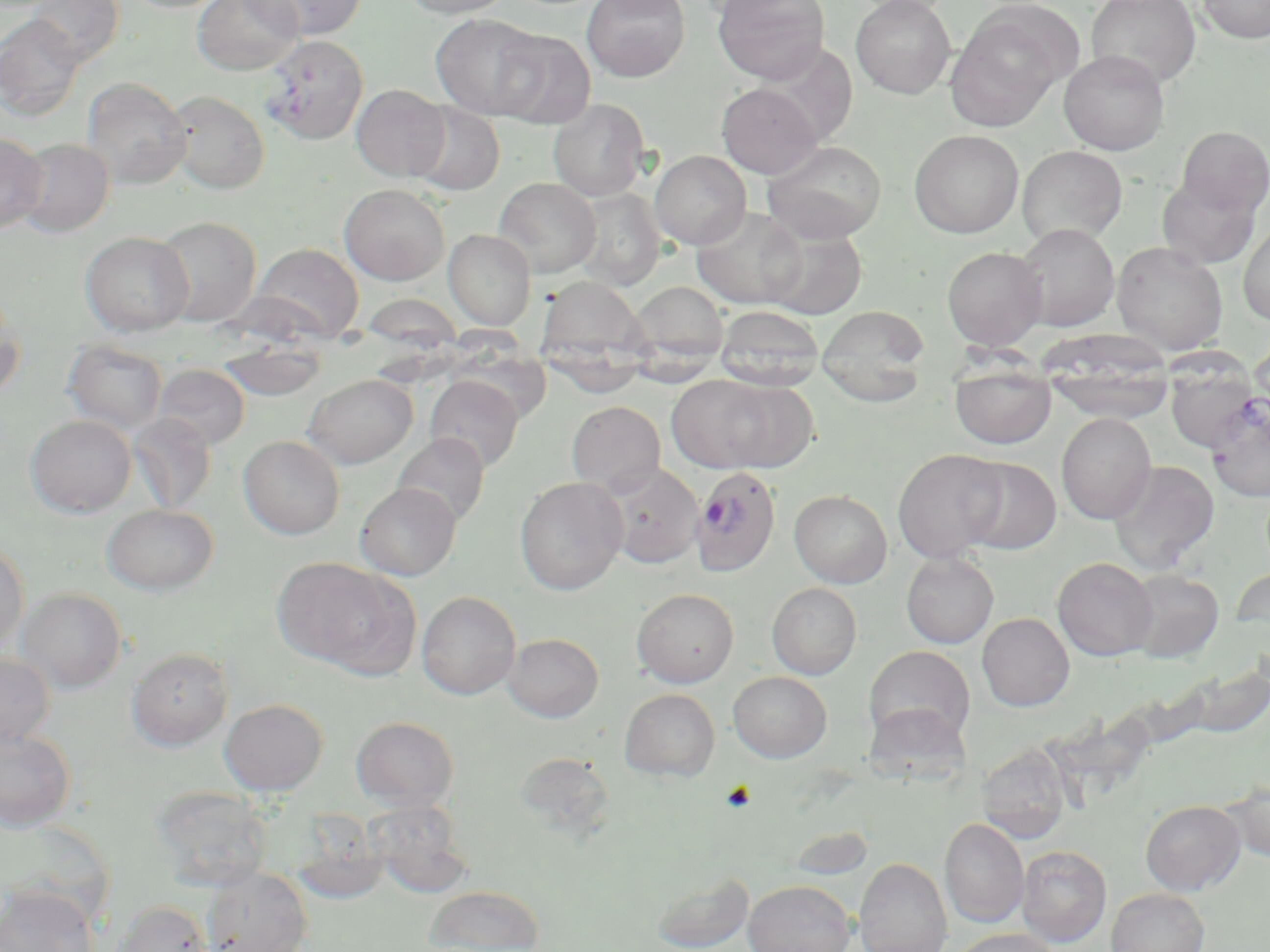

Approximate bounding boxes as named x1/y1/x2/y2 corners in pixels. Platelet locations: (x1=720, y1=781, x2=756, y2=812). Plasmodium falciparum-infected red blood cell locations: (x1=691, y1=466, x2=781, y2=576). Uninfected red blood cell locations: (x1=24, y1=0, x2=124, y2=67), (x1=193, y1=0, x2=303, y2=75), (x1=246, y1=0, x2=366, y2=40), (x1=400, y1=0, x2=514, y2=19), (x1=581, y1=0, x2=690, y2=82), (x1=594, y1=0, x2=689, y2=18), (x1=713, y1=0, x2=830, y2=84), (x1=850, y1=0, x2=956, y2=99), (x1=1087, y1=0, x2=1201, y2=89), (x1=1197, y1=0, x2=1270, y2=43), (x1=945, y1=7, x2=1072, y2=129), (x1=1, y1=13, x2=85, y2=121), (x1=430, y1=13, x2=547, y2=120), (x1=490, y1=29, x2=596, y2=129), (x1=260, y1=36, x2=368, y2=144), (x1=752, y1=48, x2=858, y2=152), (x1=1058, y1=50, x2=1170, y2=155), (x1=82, y1=78, x2=192, y2=189), (x1=717, y1=83, x2=822, y2=179), (x1=351, y1=84, x2=451, y2=181), (x1=165, y1=90, x2=270, y2=194), (x1=548, y1=99, x2=650, y2=201), (x1=409, y1=102, x2=505, y2=196), (x1=1176, y1=126, x2=1270, y2=217), (x1=909, y1=129, x2=1024, y2=238), (x1=0, y1=133, x2=48, y2=234), (x1=15, y1=138, x2=115, y2=237), (x1=762, y1=140, x2=887, y2=243), (x1=1017, y1=145, x2=1128, y2=246), (x1=650, y1=150, x2=751, y2=249), (x1=1157, y1=175, x2=1262, y2=268), (x1=493, y1=178, x2=600, y2=277), (x1=340, y1=183, x2=450, y2=285), (x1=572, y1=188, x2=665, y2=291), (x1=464, y1=197, x2=573, y2=300), (x1=692, y1=205, x2=809, y2=309), (x1=153, y1=216, x2=262, y2=326), (x1=1238, y1=222, x2=1270, y2=326), (x1=1015, y1=223, x2=1119, y2=331), (x1=762, y1=228, x2=867, y2=320), (x1=444, y1=229, x2=536, y2=330), (x1=81, y1=231, x2=194, y2=336), (x1=249, y1=242, x2=364, y2=343), (x1=1112, y1=242, x2=1228, y2=354), (x1=942, y1=246, x2=1047, y2=351), (x1=538, y1=276, x2=651, y2=370), (x1=629, y1=281, x2=730, y2=366), (x1=0, y1=291, x2=25, y2=402), (x1=816, y1=304, x2=931, y2=406), (x1=715, y1=306, x2=824, y2=391), (x1=1249, y1=329, x2=1269, y2=427), (x1=217, y1=338, x2=328, y2=401), (x1=63, y1=339, x2=167, y2=434), (x1=1040, y1=347, x2=1176, y2=423), (x1=950, y1=362, x2=1057, y2=449), (x1=153, y1=364, x2=250, y2=450), (x1=1165, y1=364, x2=1261, y2=454), (x1=304, y1=374, x2=417, y2=468), (x1=425, y1=375, x2=523, y2=472), (x1=667, y1=375, x2=781, y2=473), (x1=710, y1=380, x2=818, y2=472), (x1=1204, y1=395, x2=1270, y2=502), (x1=567, y1=401, x2=665, y2=496), (x1=1056, y1=412, x2=1156, y2=524), (x1=25, y1=414, x2=136, y2=517), (x1=128, y1=414, x2=217, y2=514), (x1=393, y1=432, x2=490, y2=528), (x1=239, y1=435, x2=345, y2=539), (x1=893, y1=449, x2=1009, y2=562), (x1=958, y1=456, x2=1060, y2=555), (x1=1108, y1=460, x2=1219, y2=574), (x1=604, y1=463, x2=703, y2=568), (x1=515, y1=476, x2=628, y2=595), (x1=355, y1=482, x2=460, y2=580), (x1=789, y1=490, x2=892, y2=588), (x1=102, y1=503, x2=218, y2=595), (x1=0, y1=538, x2=30, y2=652), (x1=901, y1=552, x2=998, y2=648), (x1=1052, y1=557, x2=1158, y2=660), (x1=277, y1=560, x2=417, y2=677), (x1=1231, y1=566, x2=1270, y2=635), (x1=1123, y1=568, x2=1224, y2=663), (x1=767, y1=583, x2=862, y2=679), (x1=17, y1=587, x2=127, y2=693), (x1=632, y1=588, x2=739, y2=688), (x1=417, y1=591, x2=521, y2=699), (x1=977, y1=613, x2=1074, y2=711), (x1=503, y1=632, x2=604, y2=722), (x1=865, y1=646, x2=975, y2=746), (x1=127, y1=647, x2=233, y2=751), (x1=0, y1=651, x2=54, y2=749), (x1=1168, y1=663, x2=1270, y2=741), (x1=728, y1=671, x2=832, y2=762), (x1=619, y1=688, x2=721, y2=781), (x1=219, y1=698, x2=328, y2=795), (x1=351, y1=716, x2=459, y2=810), (x1=0, y1=727, x2=77, y2=832), (x1=977, y1=744, x2=1072, y2=841), (x1=514, y1=751, x2=616, y2=840), (x1=1220, y1=775, x2=1270, y2=863), (x1=150, y1=785, x2=272, y2=891), (x1=364, y1=800, x2=474, y2=898), (x1=1140, y1=800, x2=1246, y2=895), (x1=940, y1=818, x2=1029, y2=928), (x1=1017, y1=845, x2=1112, y2=946), (x1=854, y1=857, x2=952, y2=952), (x1=202, y1=866, x2=313, y2=951), (x1=652, y1=872, x2=753, y2=952), (x1=743, y1=879, x2=856, y2=952), (x1=424, y1=884, x2=545, y2=952), (x1=0, y1=887, x2=100, y2=952), (x1=1107, y1=888, x2=1209, y2=951), (x1=111, y1=900, x2=213, y2=952), (x1=948, y1=927, x2=1063, y2=952). Slide-level diagnosis: Plasmodium falciparum. Thin blood smear. Light microscopy. Image is 1270×952 pixels. Captured at 1000x magnification. One field of a larger specimen. May-Grünwald-Giemsa-stained preparation.